Locate every malaria parasite.
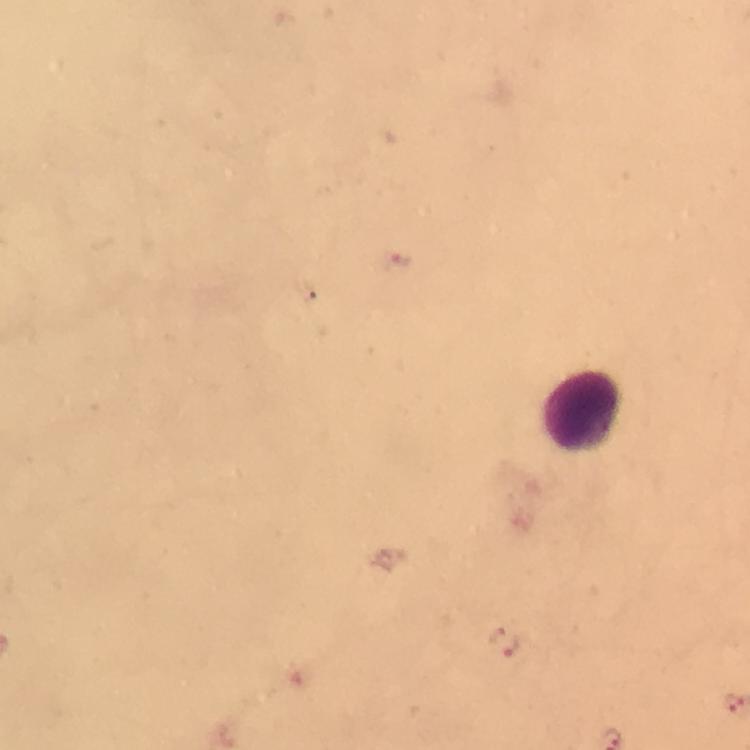

Approximate centers as (x, y) in pixels.
Malaria parasites: (400, 263), (505, 641).

Summary:
  - Leukocyte locations: (583, 412)
  - Capture: smartphone mounted on the microscope
  - Image size: 750×750 pixels
  - Magnification: 100x
  - Cropped from: one field of view
  - Immersion oil: used
  - Stain: Giemsa
  - Context: from a malaria diagnostic workup
  - Preparation: thick blood smear